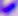 Captured at 400x magnification. Photomicrograph. Toxoplasma gondii is seen.